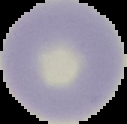 Cell region segmented out of the field of view; the surrounding area is masked to black. Malaria status: uninfected. Image is 127×124 pixels. From a thin blood smear.